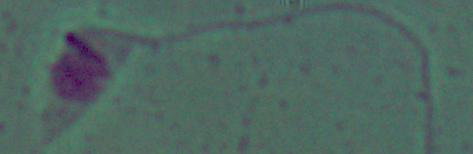
Photomicrograph. A Leishmania parasite is shown. Captured at 1000x magnification.